Look for Plasmodium parasites.
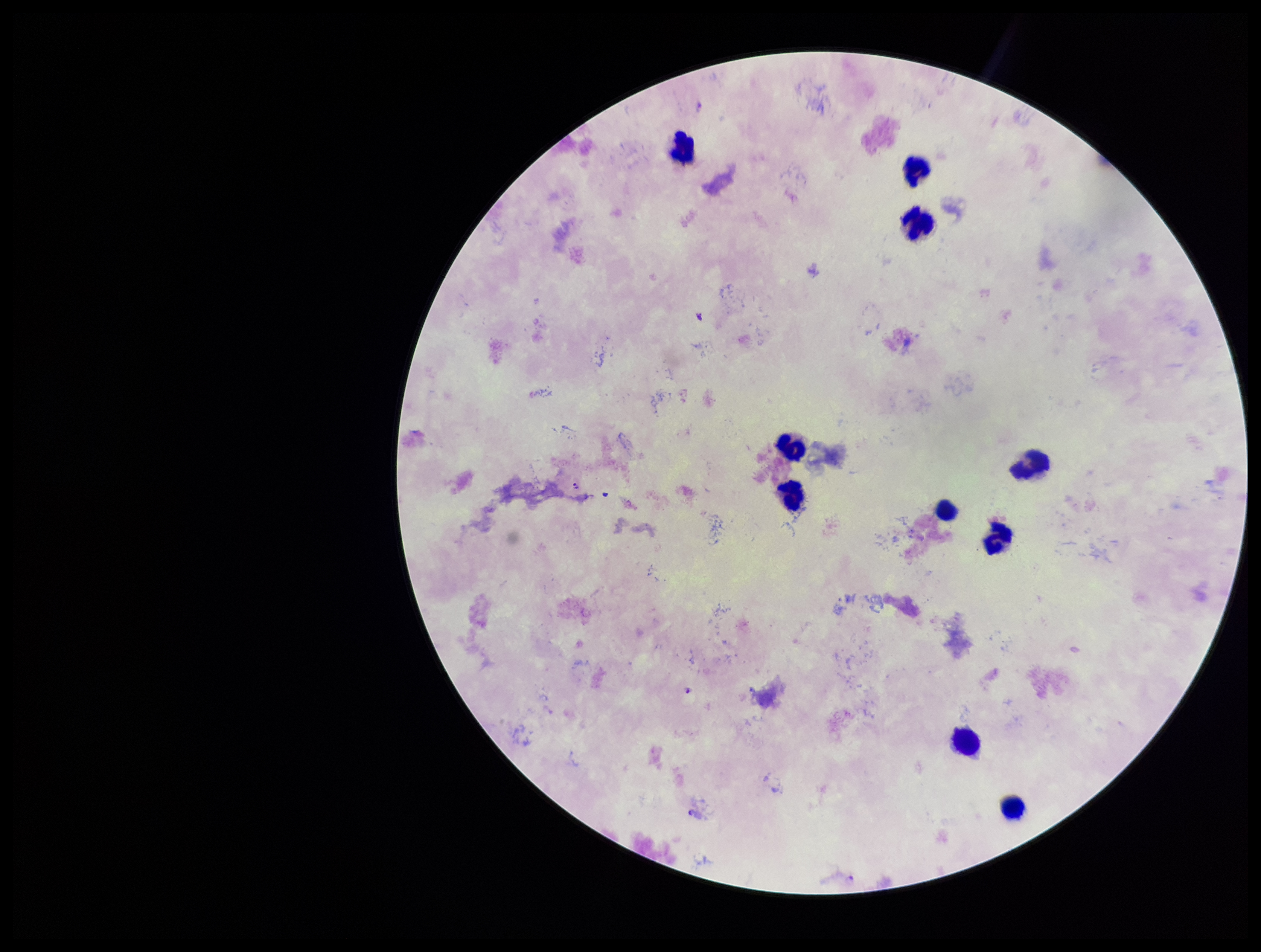

Seen.

{
  "leukocyte_count": 10,
  "parasite_count": 3,
  "image_size": "1261×952 pixels",
  "field_of_view": "single",
  "species_reported_for_this_patient": "Plasmodium falciparum",
  "stain": "Giemsa",
  "preparation": "thick blood smear",
  "patient_malaria_status": "positive",
  "capture": "smartphone photograph through the microscope eyepiece"
}